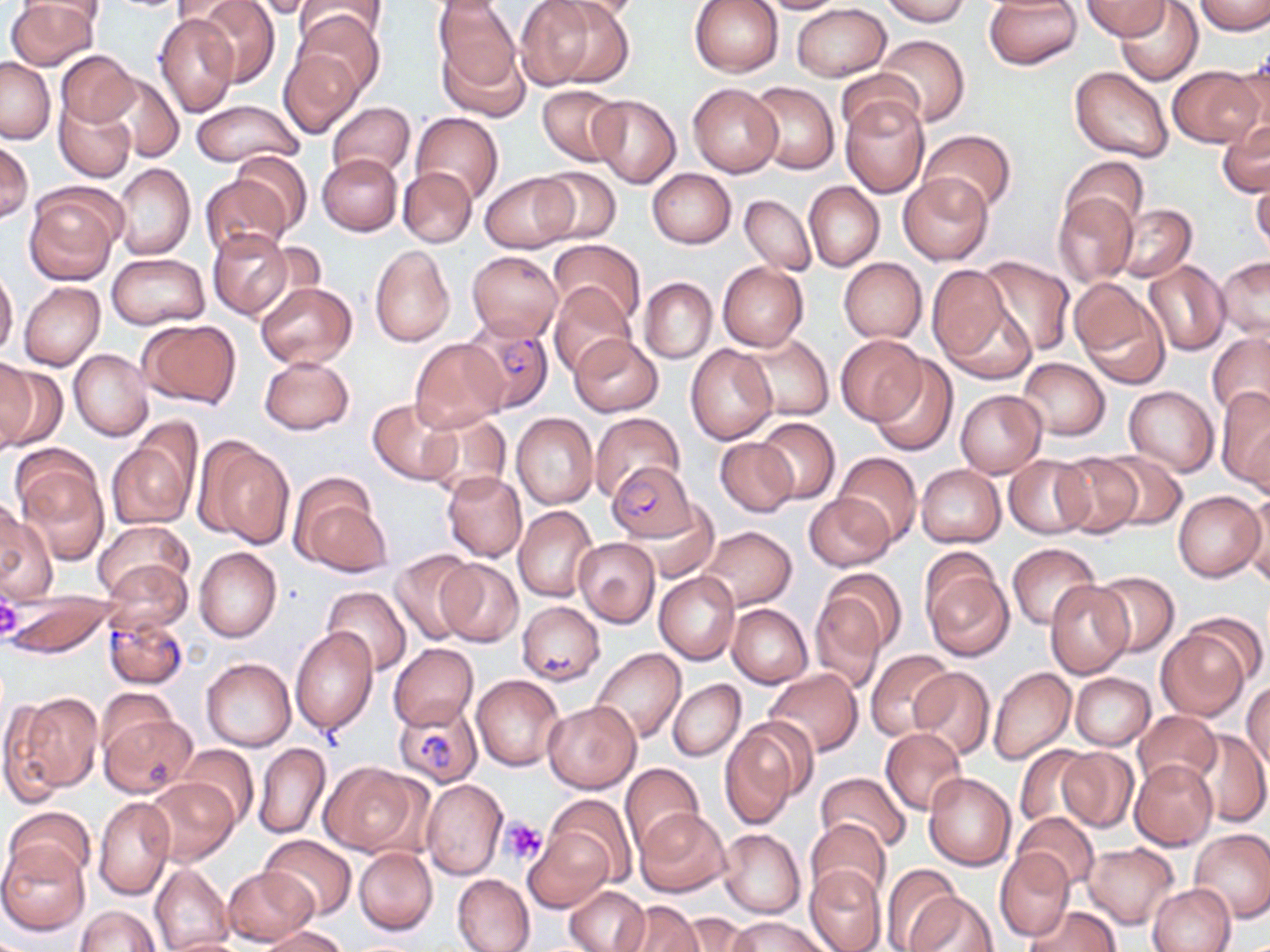
Summary:
  - Coordinate format: approximate bounding boxes as (x1, y1, x2, y2) in pixels
  - Plasmodium falciparum-infected red blood cell locations: (463, 321, 554, 413), (607, 463, 700, 542), (103, 613, 188, 688), (393, 701, 481, 794)
  - Platelet locations: (0, 595, 22, 640), (503, 817, 546, 864)
  - Uninfected red blood cell locations: (6, 0, 98, 69), (192, 0, 280, 87), (249, 0, 320, 19), (294, 0, 390, 45), (433, 0, 521, 93), (516, 0, 614, 90), (550, 0, 647, 22), (689, 0, 784, 77), (753, 0, 849, 13), (878, 0, 969, 26), (983, 1, 1082, 69), (1082, 1, 1171, 39), (1116, 1, 1203, 85), (1193, 1, 1270, 35), (791, 3, 893, 81), (295, 8, 384, 97), (154, 14, 237, 117), (874, 34, 969, 127), (440, 40, 530, 121), (279, 49, 363, 138), (55, 50, 139, 127), (1227, 57, 1270, 146), (0, 58, 54, 143), (1168, 65, 1262, 148), (1070, 66, 1174, 164), (98, 72, 183, 162), (835, 74, 927, 148), (688, 82, 782, 178), (749, 82, 837, 173), (536, 85, 625, 166), (588, 94, 681, 186), (839, 94, 931, 198), (55, 97, 136, 182), (191, 98, 304, 168), (327, 102, 415, 180), (411, 112, 502, 204), (1217, 118, 1269, 197), (921, 130, 1016, 214), (0, 141, 33, 223), (234, 149, 312, 237), (316, 153, 403, 237), (1062, 155, 1149, 234), (112, 163, 196, 260), (534, 166, 621, 245), (397, 167, 477, 248), (646, 169, 737, 249), (480, 172, 576, 253), (897, 173, 993, 265), (199, 174, 295, 260), (1252, 175, 1270, 258), (804, 181, 884, 272), (25, 191, 120, 284), (739, 194, 815, 276), (1054, 194, 1137, 286), (1113, 204, 1196, 282), (207, 228, 294, 321), (549, 239, 646, 328), (369, 245, 456, 347), (466, 250, 563, 343), (107, 252, 209, 329), (979, 255, 1075, 355), (1216, 257, 1269, 340), (838, 258, 927, 343), (1144, 260, 1229, 357), (717, 263, 808, 351), (926, 264, 1016, 369), (0, 268, 18, 359), (639, 277, 716, 363), (19, 281, 104, 371), (255, 281, 356, 370), (1071, 281, 1168, 385), (548, 282, 636, 376), (137, 319, 241, 409), (1207, 332, 1270, 422), (742, 333, 834, 421), (568, 334, 663, 417), (835, 335, 927, 426), (409, 338, 509, 432), (686, 345, 778, 444), (69, 349, 153, 441), (259, 355, 354, 436), (871, 357, 958, 457), (1016, 357, 1109, 441), (0, 361, 63, 452), (1217, 385, 1270, 487), (1124, 386, 1219, 476), (956, 390, 1047, 478), (368, 399, 460, 485), (421, 412, 511, 500), (590, 412, 683, 502), (512, 413, 597, 509), (753, 417, 839, 504), (105, 436, 196, 530), (197, 437, 295, 550), (714, 437, 798, 517), (1101, 451, 1186, 530), (833, 452, 921, 546), (1052, 452, 1144, 537), (1004, 455, 1095, 539), (16, 460, 109, 562), (916, 464, 1005, 547), (442, 471, 527, 562), (289, 476, 388, 576), (1242, 489, 1269, 587), (1173, 490, 1265, 581), (802, 492, 897, 572), (639, 504, 718, 581), (1, 505, 59, 604), (513, 506, 597, 602), (94, 519, 194, 602), (699, 525, 798, 611), (573, 538, 660, 627), (1007, 543, 1099, 629), (195, 547, 282, 642), (389, 550, 479, 646), (919, 557, 1013, 662), (103, 559, 193, 636), (437, 559, 523, 646), (819, 568, 906, 655), (1090, 571, 1180, 656), (654, 572, 740, 664), (1045, 582, 1134, 678), (322, 585, 411, 677), (808, 592, 888, 691), (6, 595, 115, 659), (517, 600, 605, 686), (726, 603, 812, 687), (1185, 611, 1267, 687), (1155, 626, 1251, 720), (290, 627, 378, 737), (389, 643, 478, 731), (592, 648, 686, 743), (865, 649, 956, 740), (201, 656, 297, 752), (910, 666, 994, 758), (989, 667, 1076, 764), (763, 670, 863, 757), (1070, 672, 1155, 750), (471, 675, 565, 771), (668, 679, 745, 761), (1243, 682, 1270, 770), (8, 691, 103, 796), (97, 691, 178, 758), (543, 700, 642, 793), (1133, 710, 1220, 789), (100, 711, 198, 798), (718, 726, 805, 829), (881, 727, 967, 816), (1188, 729, 1270, 827), (254, 742, 330, 840), (1014, 743, 1095, 829), (177, 744, 259, 827), (1057, 747, 1138, 832), (1129, 760, 1217, 850), (320, 761, 425, 857), (620, 763, 705, 852), (816, 772, 912, 854), (924, 773, 1017, 870), (143, 777, 240, 867), (422, 779, 508, 879), (548, 794, 636, 884), (94, 797, 176, 900), (4, 806, 94, 883), (635, 808, 732, 898), (1012, 812, 1100, 891), (806, 819, 891, 902), (718, 829, 806, 918), (523, 830, 611, 911), (1190, 830, 1270, 924), (259, 834, 356, 920), (0, 842, 88, 935), (1083, 843, 1179, 928), (354, 848, 437, 935), (994, 849, 1075, 941), (150, 864, 232, 950), (804, 864, 887, 952), (224, 867, 318, 945), (883, 868, 965, 952), (453, 874, 535, 952), (1148, 883, 1236, 952), (564, 885, 648, 952), (907, 890, 996, 952), (616, 900, 702, 951), (75, 905, 161, 952), (1024, 905, 1121, 952), (672, 913, 754, 952), (729, 915, 829, 952), (261, 925, 347, 952), (162, 936, 250, 952)
  - Slide-level diagnosis: Plasmodium falciparum
  - Stain: May-Grünwald-Giemsa
  - Field of view: one of a larger specimen
  - Magnification: 1000x
  - Image size: 1270×952 pixels
  - Modality: optical microscopy
  - Preparation: thin blood film